Report the malaria status of this cell.
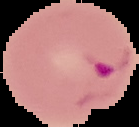

It is parasitized.

Image is 139×127 pixels. From a thin blood smear. Cell region segmented out of the field of view; the surrounding area is masked to black.